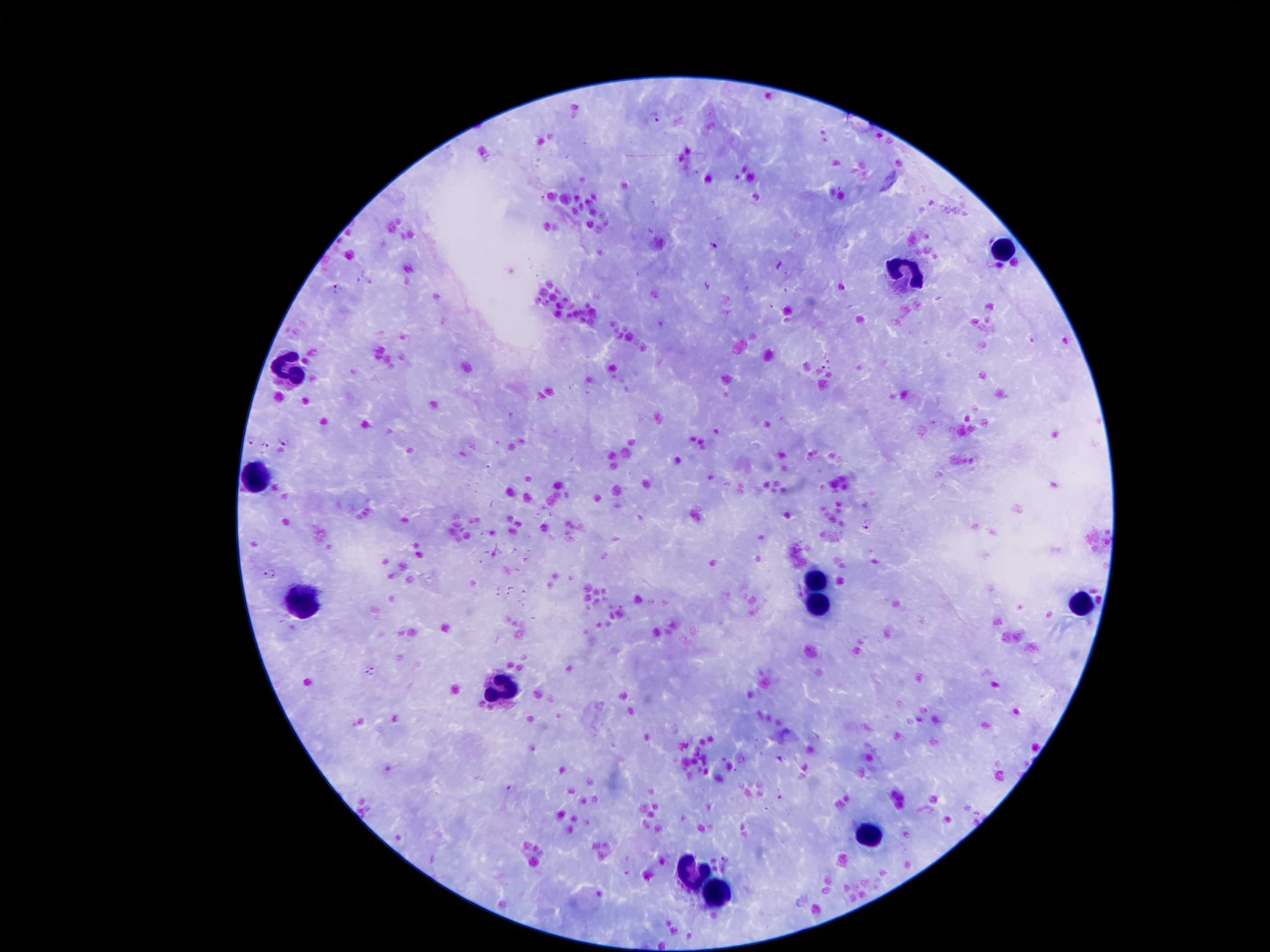
coordinate format = approximate centers as [x, y] in pixels
leukocyte locations = [1001, 249], [908, 279], [289, 372], [250, 478], [816, 578], [1079, 604], [303, 607], [819, 607], [499, 693], [869, 837], [690, 876], [715, 896]
Plasmodium parasite locations = [655, 117], [715, 246], [779, 266], [708, 284], [337, 288], [825, 367], [250, 440], [284, 441], [265, 447], [867, 524], [370, 670], [510, 789], [780, 796], [629, 872]
capture = smartphone camera through the microscope eyepiece
preparation = thick blood smear
field of view = one from this slide
stain = Giemsa
patient malaria status = infected with Plasmodium falciparum
magnification = 100x
image size = 1270×952 pixels